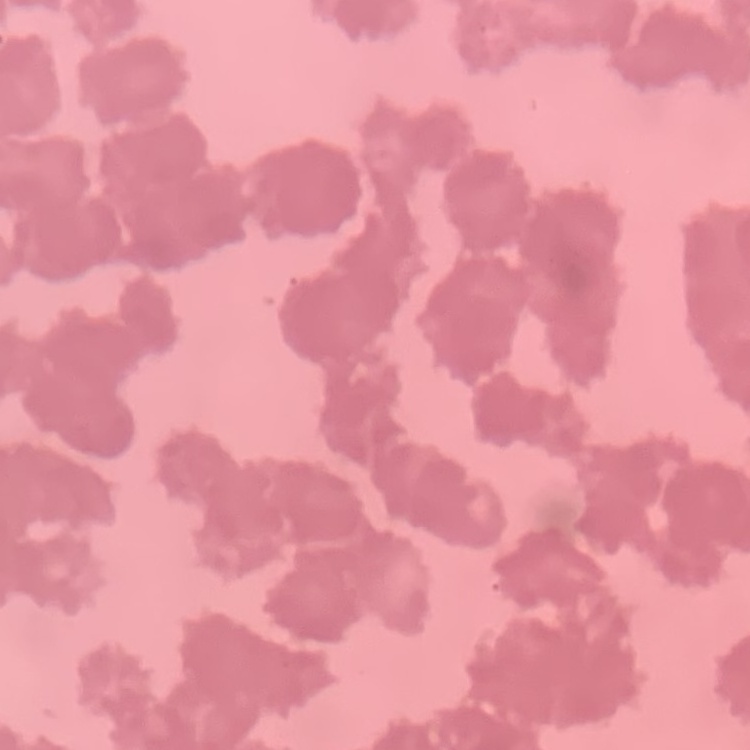

Summary:
  - Red blood cell morphology: rouleaux formation
  - Stain: Field's or Giemsa
  - Preparation: thin blood smear
  - Image type: one tile cut from a larger photomicrograph